Outline each Plasmodium ovale-infected red blood cell.
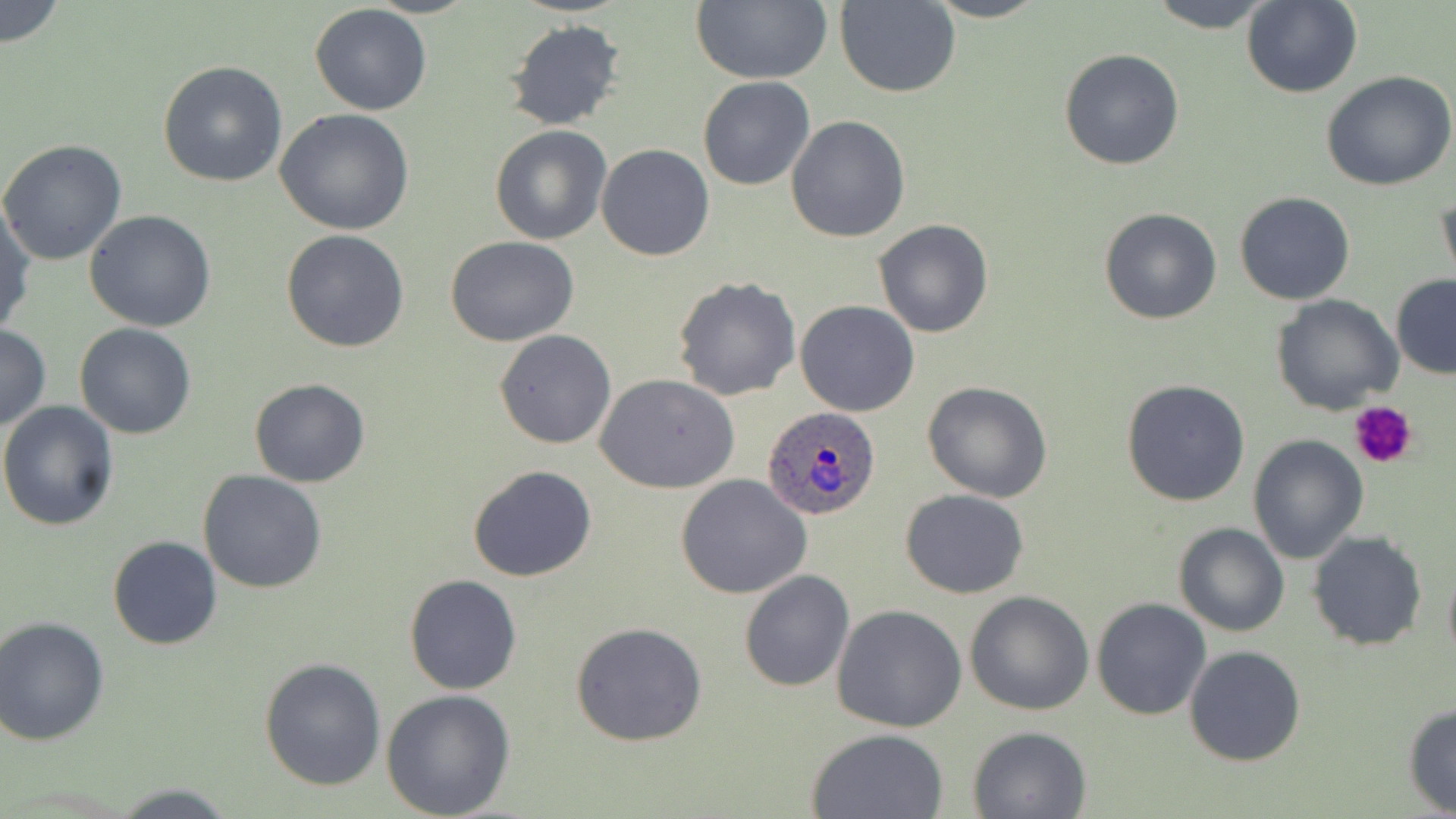

Approximate bounding boxes as (x1,y1)-(x2,y2) corner pairs in pixels.
Plasmodium ovale-infected red blood cells: (762,406)-(882,521).

Platelet locations: (1348,400)-(1418,471). Uninfected red blood cell locations: (1,0)-(65,49), (688,0)-(834,86), (923,0)-(1049,23), (1146,0)-(1279,33), (834,1)-(961,97), (1241,1)-(1364,99), (310,4)-(432,115), (504,18)-(627,133), (1058,47)-(1185,170), (158,60)-(288,187), (1322,71)-(1456,191), (697,76)-(816,191), (274,108)-(415,235), (786,116)-(910,241), (489,124)-(612,245), (0,138)-(127,266), (595,145)-(714,262), (1436,187)-(1456,294), (1234,191)-(1355,306), (0,202)-(36,338), (1098,208)-(1223,326), (84,210)-(218,331), (873,219)-(994,338), (281,228)-(410,352), (446,235)-(580,347), (1390,274)-(1456,378), (673,276)-(802,401), (1271,294)-(1402,415), (795,300)-(919,417), (74,322)-(197,440), (0,325)-(50,433), (494,329)-(617,448), (595,375)-(739,494), (1120,378)-(1251,506), (250,379)-(372,488), (922,381)-(1054,503), (0,402)-(121,533), (1247,434)-(1368,564), (467,465)-(597,582), (198,471)-(328,592), (676,474)-(812,599), (901,489)-(1030,599), (1172,522)-(1289,637), (1307,531)-(1428,651), (107,535)-(222,650), (1442,554)-(1456,668), (738,570)-(855,693), (404,574)-(522,694), (964,591)-(1093,716), (1091,597)-(1212,720), (832,604)-(967,734), (0,615)-(110,746), (572,620)-(705,747), (1184,645)-(1306,767), (259,658)-(386,790), (380,687)-(516,818), (1402,702)-(1456,816), (967,724)-(1093,818), (806,727)-(949,818), (108,783)-(237,816). Slide-level diagnosis: Plasmodium ovale. Light microscopy. One field of a larger specimen. 1000x magnification. Image is 1456×819 pixels. Thin blood film. May-Grünwald-Giemsa-stained preparation.